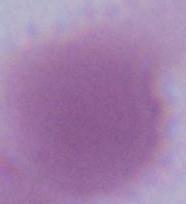

magnification: 1000x
modality: photomicrograph
identification: red blood cell